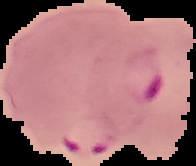
preparation = thin blood smear
result = Plasmodium parasites detected
image size = 196×166 pixels
image type = segmented cell region with the area outside set to black